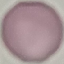

Summary:
  - Malaria status: uninfected
  - Image type: cell patch, automatically extracted from a larger field of view and resized to 64 × 64 pixels
  - Stain: Giemsa
  - Capture: smartphone through the microscope eyepiece
  - Preparation: thin blood smear